Give the preparation type.
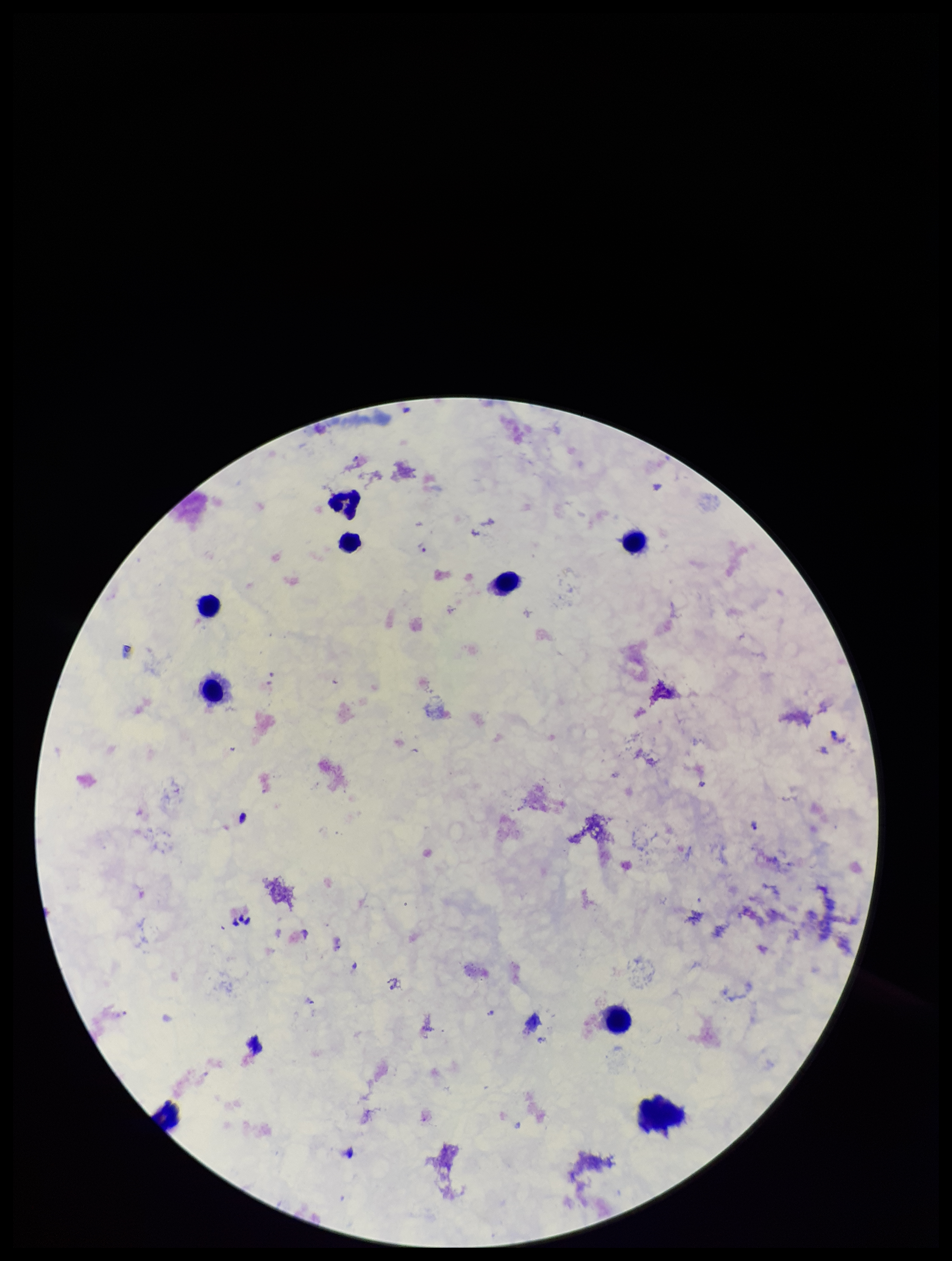

It is a thick blood smear.

field of view = one from this slide
species reported for this patient = Plasmodium falciparum
stain = Giemsa
patient malaria status = positive
Plasmodium parasites = detected
capture = smartphone photograph through the microscope eyepiece
leukocyte count = 9
parasite count = 3
image size = 952×1261 pixels